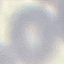

Summary:
  - Result: no malaria parasites detected
  - Stain: Giemsa
  - Image type: cell patch, automatically extracted from a larger field of view and resized to 64 × 64 pixels
  - Preparation: thin smear
  - Capture: smartphone camera at the microscope eyepiece